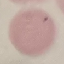 Malaria status: uninfected. Thin blood smear. Acquired by smartphone through the microscope eyepiece. Automatically extracted cell patch, resized to 64 × 64 pixels. Giemsa-stained preparation.